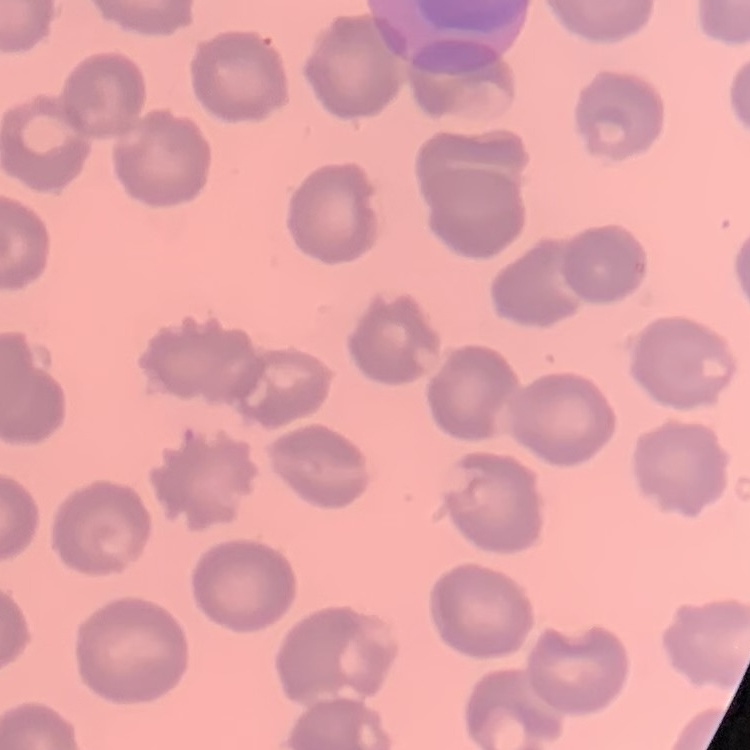
erythrocyte_morphology: no rouleaux formation
image_type: one tile cut from a larger photomicrograph
preparation: thin peripheral smear
stain: Field's or Giemsa